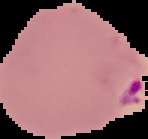

From a thin blood film. Malaria status: parasitized. Segmented cell region on a black background. Image is 148×139 pixels.